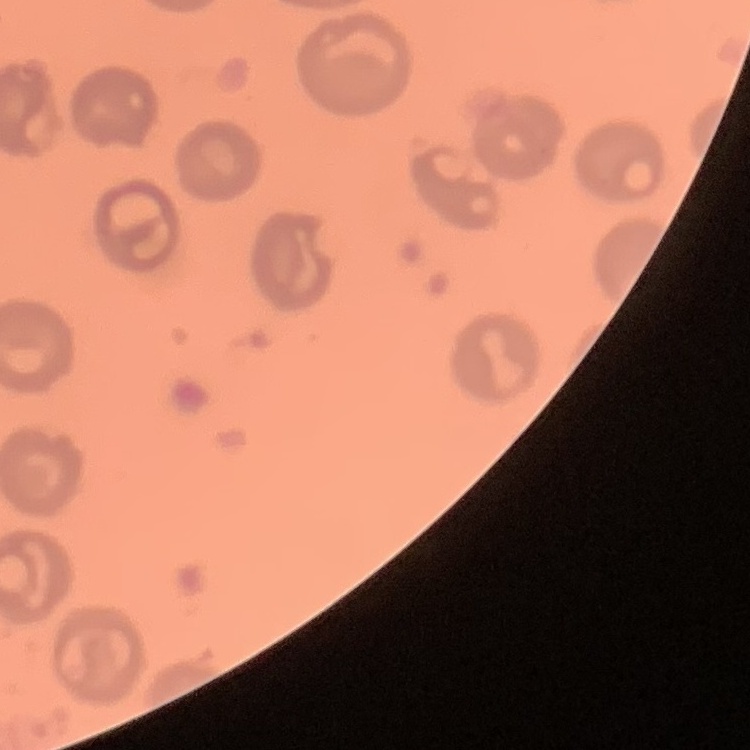 The red blood cells exhibit no rouleaux formation. One tile cut from a larger photomicrograph. Stained with either Field's or Giemsa. Thin peripheral smear.